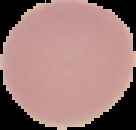
Result: no malaria parasites seen. Image is 136×130 pixels. From a thin blood film. The area outside the segmented cell region is set to black.